Classify this cell by malaria status.
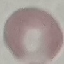

Uninfected.

Thin blood smear. Giemsa stain. Cell patch, automatically extracted from a larger field of view and resized to 64 × 64 pixels. Photographed with a smartphone camera at the microscope eyepiece.